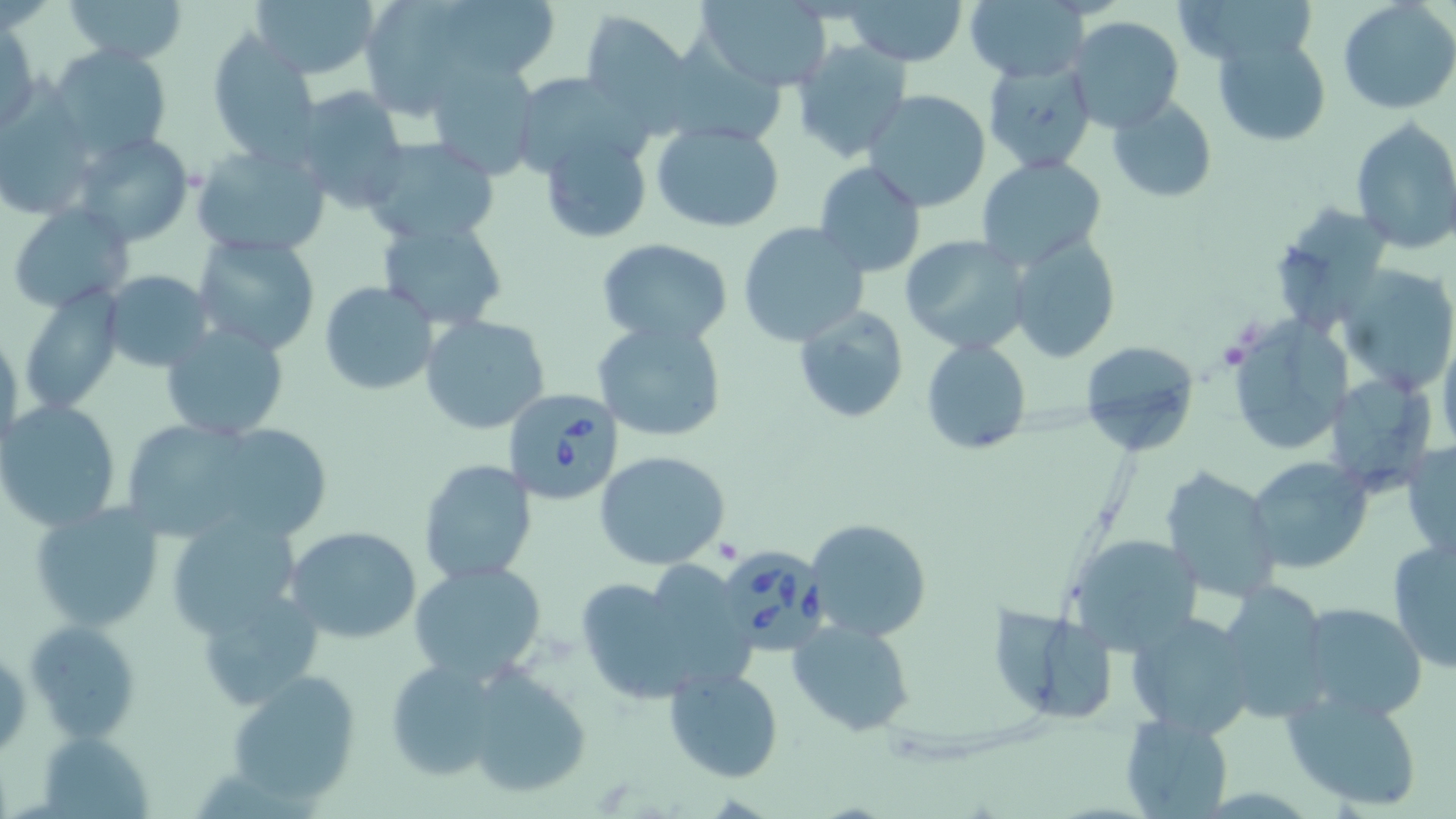

slide-level diagnosis = Babesia divergens
stain = May-Grünwald-Giemsa
modality = optical microscopy
image size = 1456×819 pixels
uninfected red blood cell locations = approximate bounding boxes as [x1, y1, x2, y2] in pixels: [60, 0, 189, 65], [251, 0, 382, 82], [358, 0, 532, 122], [439, 0, 560, 71], [694, 0, 836, 92], [965, 0, 1089, 81], [1185, 0, 1318, 69], [843, 1, 969, 65], [1338, 1, 1456, 115], [579, 9, 693, 119], [1064, 17, 1185, 136], [2, 21, 40, 134], [206, 33, 319, 161], [1212, 35, 1332, 147], [793, 38, 911, 162], [670, 41, 792, 145], [46, 44, 173, 162], [982, 59, 1099, 175], [425, 60, 540, 179], [509, 73, 647, 179], [290, 86, 411, 214], [863, 88, 994, 212], [0, 95, 101, 220], [1105, 96, 1216, 203], [1350, 117, 1456, 254], [650, 121, 785, 232], [539, 131, 653, 243], [68, 132, 195, 248], [358, 137, 501, 245], [191, 142, 331, 261], [975, 155, 1107, 271], [813, 161, 926, 278], [7, 203, 135, 312], [1267, 206, 1393, 338], [376, 216, 511, 332], [737, 221, 871, 347], [1007, 232, 1121, 362], [901, 234, 1030, 354], [193, 235, 320, 354], [596, 237, 732, 347], [1337, 262, 1456, 396], [100, 270, 214, 371], [319, 281, 439, 396], [17, 287, 124, 415], [791, 303, 909, 424], [420, 314, 551, 435], [593, 320, 726, 445], [161, 322, 289, 441], [1229, 322, 1357, 457], [1439, 325, 1456, 457], [1, 326, 23, 457], [921, 339, 1032, 454], [1078, 342, 1201, 455], [1321, 372, 1437, 494], [0, 398, 122, 531], [134, 424, 252, 537], [222, 431, 332, 541], [1404, 439, 1455, 562], [595, 451, 730, 569], [1244, 455, 1372, 575], [417, 458, 538, 585], [1158, 465, 1281, 599], [29, 501, 165, 632], [161, 510, 306, 635], [803, 519, 932, 642], [284, 524, 422, 644], [1064, 532, 1204, 653], [1386, 534, 1455, 674], [406, 559, 550, 684], [574, 567, 727, 704], [1216, 577, 1334, 725], [192, 580, 329, 709], [1295, 601, 1428, 720], [992, 602, 1120, 728], [1124, 610, 1258, 740], [24, 618, 144, 744], [788, 618, 915, 737], [380, 657, 515, 782], [454, 664, 596, 801], [663, 667, 783, 783], [225, 669, 363, 806], [1282, 685, 1427, 811], [1120, 711, 1233, 817]
preparation = thin blood film
field of view = one of a larger specimen
Babesia divergens-infected red blood cell locations = approximate bounding boxes as [x1, y1, x2, y2] in pixels: [503, 386, 625, 505], [716, 545, 828, 655]
magnification = 1000x